State which parasite is depicted.
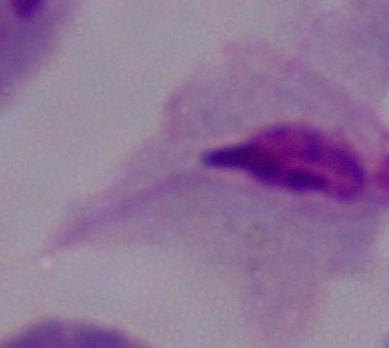

This is a trichomonad.

Summary:
  - Magnification: 1000x
  - Modality: photomicrograph